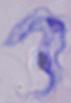

Summary:
  - Identification: trypanosome
  - Modality: micrograph
  - Magnification: 1000x